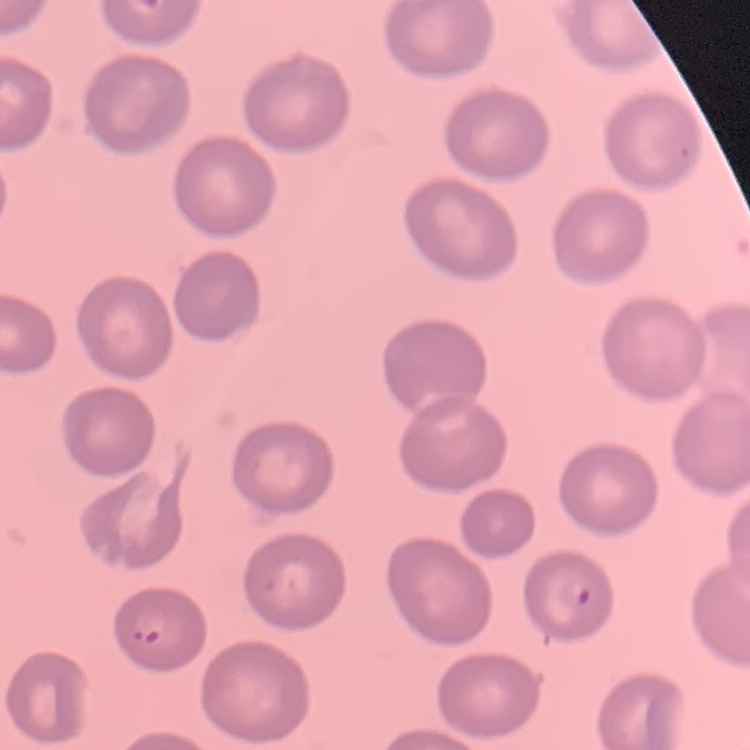 The erythrocytes show no rouleaux formation. Square crop of a larger photomicrograph. Thin blood film. Stained with either Field's or Giemsa.